Assess this cell for malaria.
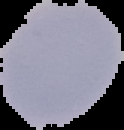
Uninfected.

Summary:
  - Image type: cell region segmented out of the field of view; surrounding area masked to black
  - Preparation: thin blood film
  - Image size: 124×130 pixels